Classify this cell by malaria status.
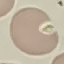
Uninfected.

image_type: cell patch, automatically extracted from a larger field of view and resized to 64 × 64 pixels
preparation: thin blood smear
stain: Giemsa
capture: smartphone through the microscope eyepiece